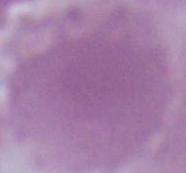

modality = micrograph
magnification = 1000x
identification = erythrocyte